Describe the morphology of the red blood cells.
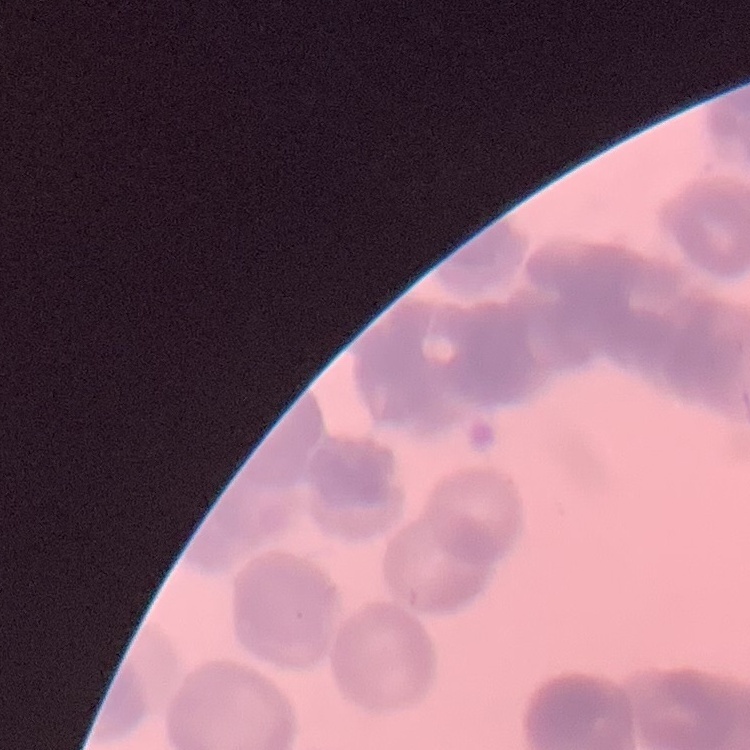

Rouleaux formation.

Summary:
  - Stain: Field's or Giemsa
  - Image type: square crop of a larger photomicrograph
  - Preparation: thin blood film